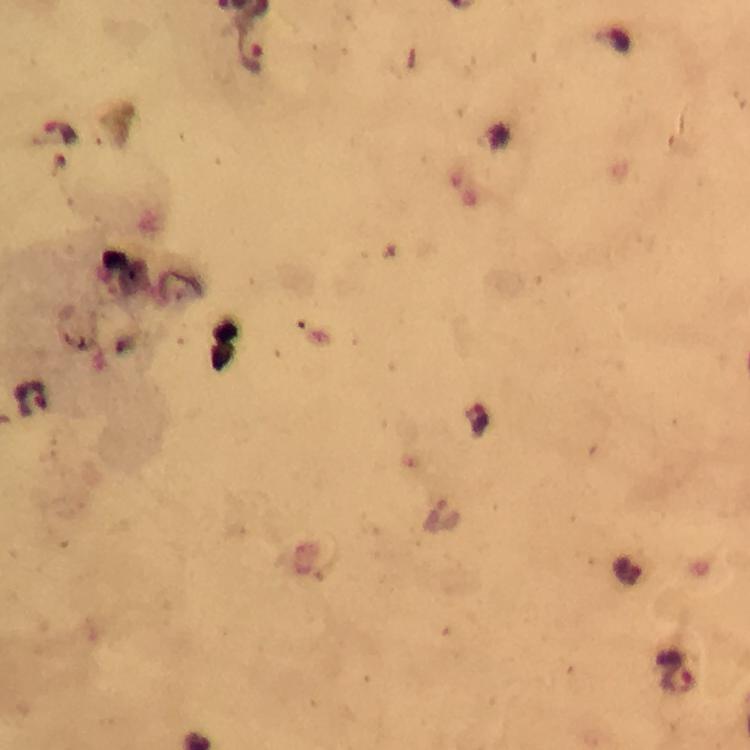
{
  "cropped_from": "one field of view",
  "preparation": "thick smear",
  "context": "from a malaria diagnostic workup",
  "stain": "Giemsa",
  "image_size": "750×750 pixels",
  "immersion_oil": "used",
  "plasmodium_parasite_locations": "approximate centers as {x, y} in pixels: {250, 52}, {60, 132}, {33, 400}, {680, 683}",
  "magnification": "100x",
  "capture": "smartphone mounted on the microscope"
}